Identify the blood parasite species.
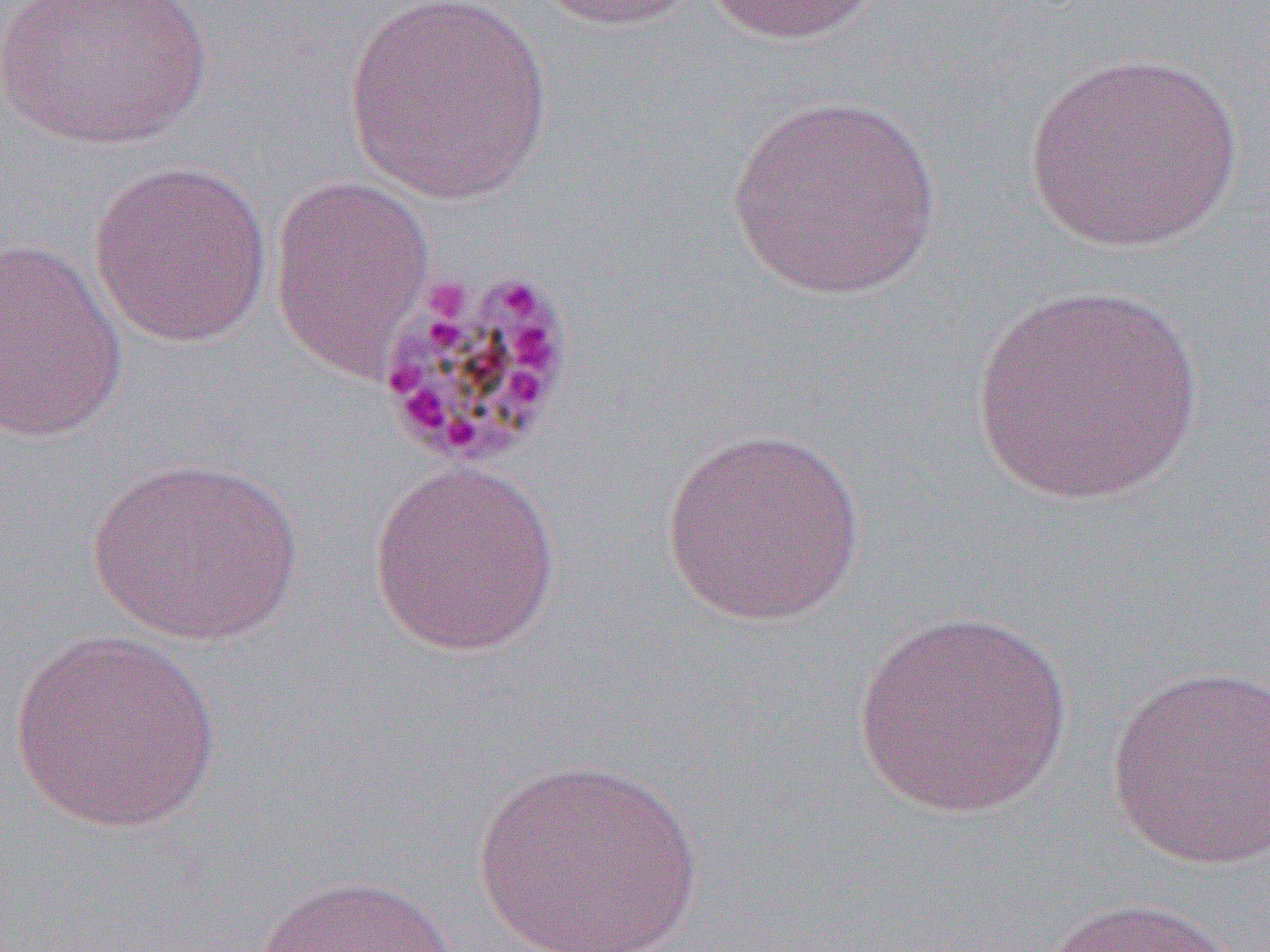

Plasmodium malariae.

uninfected red blood cell locations = approximate bounding boxes as (x1, y1, x2, y2) in pixels: (1, 0, 215, 150), (533, 0, 699, 32), (699, 0, 884, 46), (341, 1, 558, 206), (1022, 52, 1243, 254), (723, 95, 944, 301), (88, 159, 274, 349), (268, 174, 437, 381), (0, 238, 128, 443), (971, 283, 1204, 506), (659, 426, 869, 627), (86, 456, 305, 646), (367, 460, 563, 658), (853, 608, 1074, 819), (7, 629, 225, 835), (1104, 665, 1270, 869), (472, 755, 705, 951), (255, 873, 460, 952), (1041, 895, 1247, 952)
modality = optical microscopy
preparation = thin blood smear
Plasmodium malariae-infected red blood cell locations = approximate bounding boxes as (x1, y1, x2, y2) in pixels: (373, 263, 581, 473)
image size = 1270×952 pixels
magnification = 1000x
field of view = one of a larger specimen